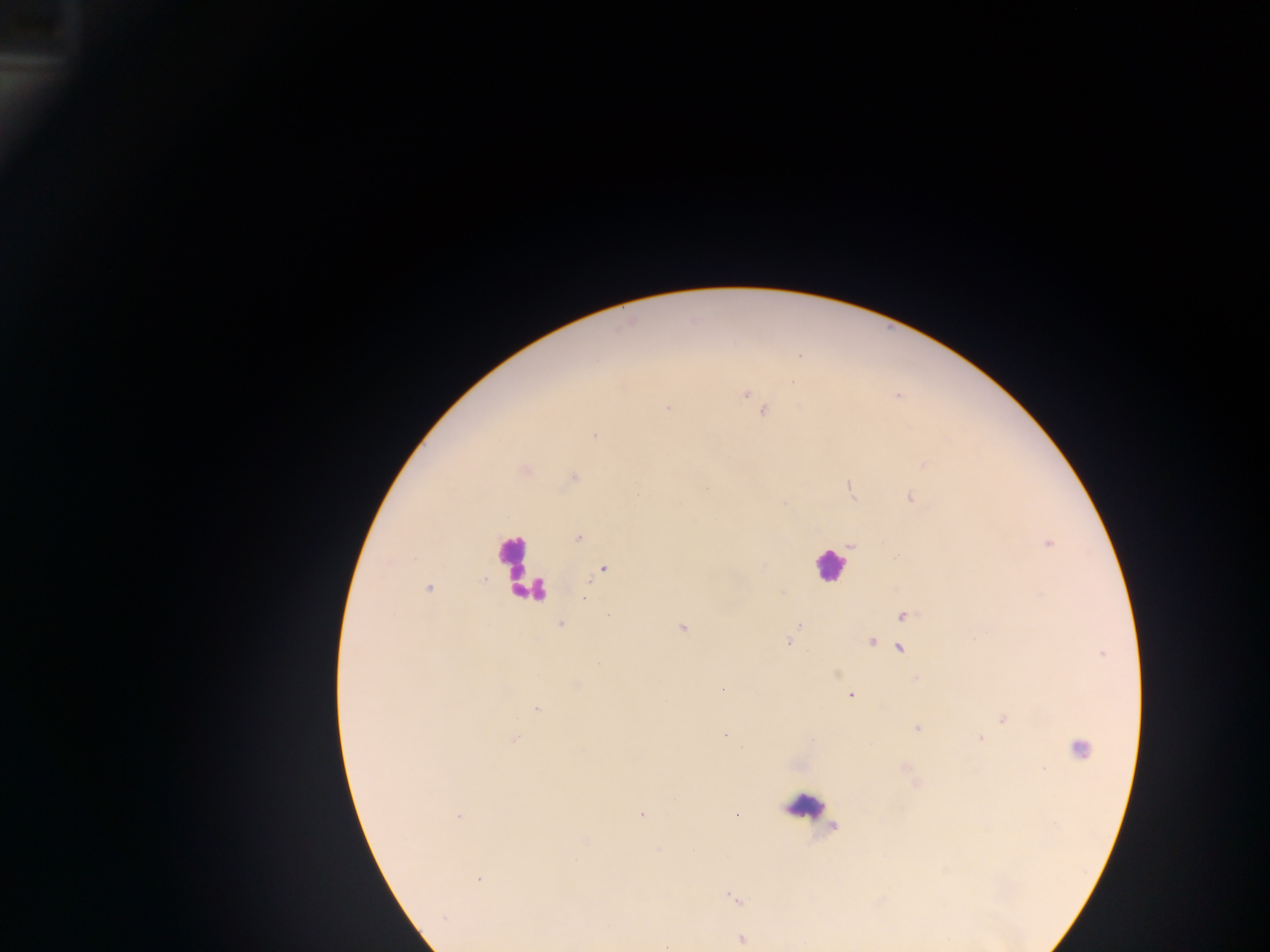
country = Ghana
capture = mobile-phone photograph through a microscope
leukocyte locations = approximate centers as {x, y} in pixels: {511, 556}, {828, 565}, {530, 585}, {809, 808}
field of view = single
Plasmodium parasite locations = approximate centers as {x, y} in pixels: {744, 395}, {668, 408}, {763, 411}, {595, 436}, {574, 477}, {851, 488}, {911, 498}, {578, 538}, {1049, 544}, {851, 545}, {602, 571}, {429, 588}, {903, 616}, {560, 625}, {798, 625}, {682, 628}, {788, 643}, {871, 643}, {900, 648}, {722, 688}, {851, 695}, {536, 709}, {1003, 720}, {917, 728}, {725, 735}, {980, 738}, {514, 739}, {1080, 748}, {641, 814}, {459, 816}, {478, 879}, {733, 899}, {444, 918}, {741, 939}
preparation = thick blood film
image size = 1270×952 pixels